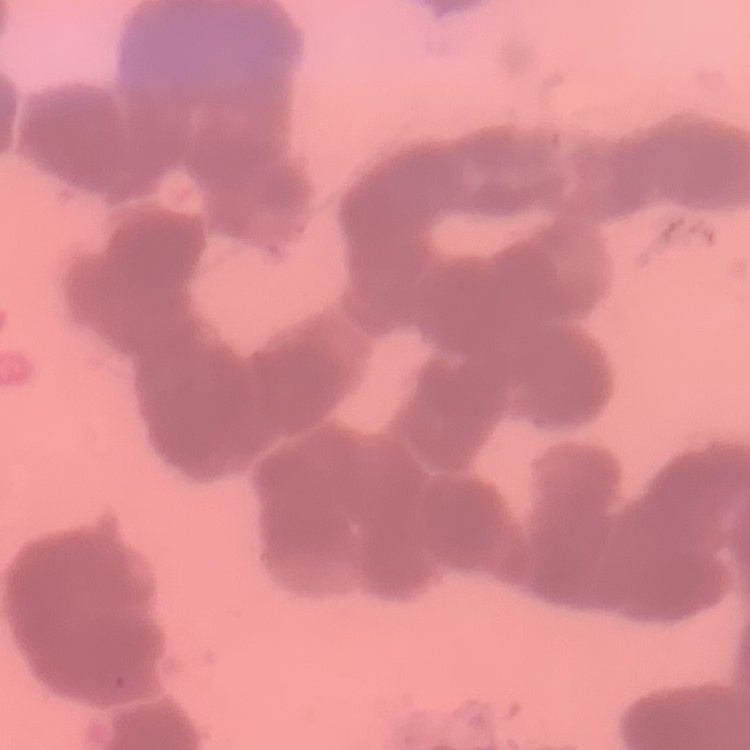
The erythrocytes exhibit rouleaux formation. Field's or Giemsa stain. Square crop of a larger photomicrograph. Thin blood film.